Describe the morphology of the red blood cells.
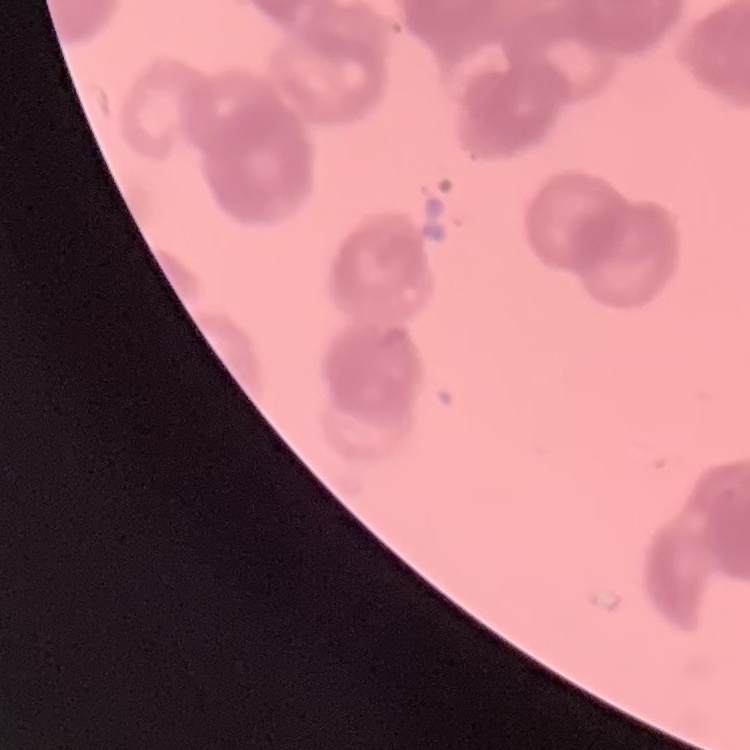

They show rouleaux formation.

{
  "image_type": "one tile cut from a larger photomicrograph",
  "preparation": "thin blood film",
  "stain": "Field's or Giemsa"
}